Give the preparation type.
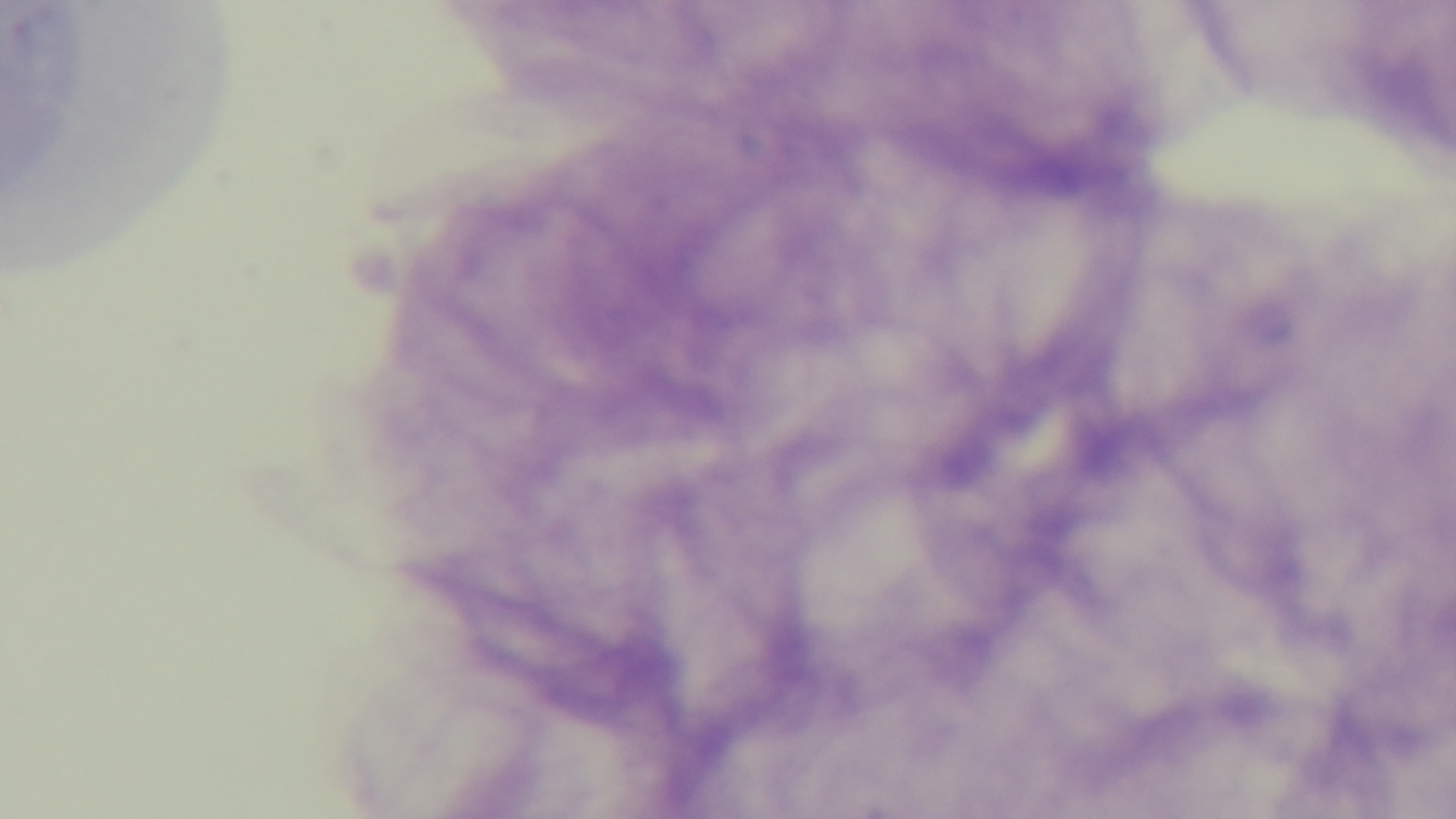

It is a thick blood film.

capture = mounted 4K digital camera
modality = light microscopy
malaria status = negative
field of view = single
stain = Giemsa
objective = 100x oil immersion